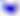
Photomicrograph. Toxoplasma gondii is shown. Captured at 400x magnification.